Locate the Plasmodium falciparum-infected red blood cells and any of indeterminate infection status.
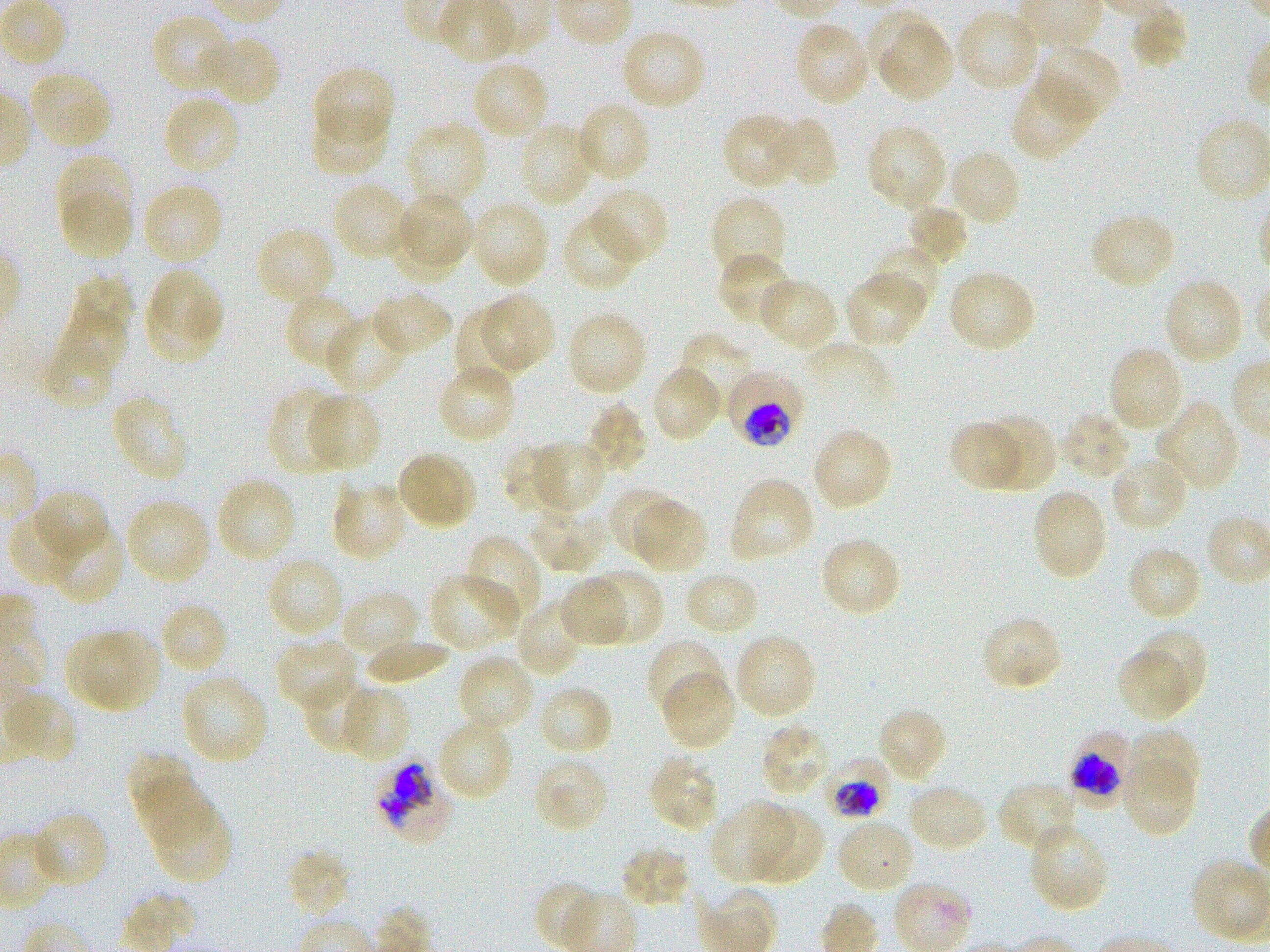
Approximate bounding boxes as {x1, y1, x2, y2} in pixels. Not every red blood cell is marked. A life-cycle stage — or a range of stages, where the recorded stages span more than one — follows each staged infected red blood cell.
Infected red blood cells: {726, 368, 806, 450} trophozoite; {1072, 727, 1135, 809}; {822, 755, 894, 821} trophozoite; {373, 758, 453, 845}.
Red blood cells of indeterminate infection status: {835, 818, 916, 895}.

{
  "locations_of_uninfected_red_blood_cells": "{1129, 7, 1189, 70}, {956, 9, 1041, 92}, {864, 10, 936, 81}, {151, 14, 234, 94}, {793, 21, 871, 107}, {875, 21, 955, 102}, {620, 28, 707, 111}, {201, 34, 281, 108}, {1036, 45, 1123, 125}, {471, 60, 551, 142}, {312, 67, 396, 144}, {27, 70, 113, 149}, {1011, 76, 1095, 161}, {162, 95, 241, 176}, {575, 101, 652, 183}, {310, 104, 391, 177}, {720, 113, 800, 189}, {770, 116, 838, 189}, {404, 119, 489, 208}, {517, 122, 596, 208}, {865, 125, 948, 213}, {948, 148, 1022, 227}, {55, 155, 132, 229}, {332, 181, 409, 262}, {142, 182, 224, 265}, {58, 187, 133, 260}, {590, 187, 669, 264}, {396, 190, 474, 269}, {709, 194, 788, 280}, {471, 200, 550, 287}, {904, 202, 971, 267}, {562, 212, 641, 292}, {1089, 212, 1177, 291}, {394, 218, 457, 285}, {254, 227, 337, 307}, {871, 245, 942, 315}, {716, 253, 794, 326}, {947, 268, 1036, 354}, {149, 269, 224, 340}, {845, 272, 927, 348}, {70, 273, 134, 336}, {757, 277, 839, 352}, {1162, 277, 1245, 366}, {370, 289, 453, 357}, {285, 294, 364, 371}, {480, 294, 556, 374}, {146, 298, 218, 363}, {56, 306, 127, 375}, {452, 307, 519, 383}, {565, 309, 649, 396}, {324, 312, 407, 394}, {676, 334, 752, 412}, {38, 339, 116, 411}, {805, 341, 892, 420}, {1107, 345, 1185, 433}, {436, 363, 517, 445}, {650, 365, 723, 445}, {268, 388, 348, 477}, {307, 391, 383, 472}, {110, 394, 190, 483}, {1154, 400, 1239, 493}, {584, 401, 648, 475}, {1058, 410, 1131, 481}, {983, 413, 1058, 491}, {948, 420, 1024, 492}, {811, 427, 894, 511}, {530, 440, 607, 515}, {500, 441, 565, 513}, {397, 451, 477, 531}, {1110, 455, 1189, 532}, {215, 476, 297, 564}, {729, 477, 815, 562}, {330, 479, 408, 562}, {606, 486, 680, 559}, {1030, 487, 1109, 581}, {33, 490, 110, 562}, {124, 498, 212, 585}, {632, 500, 707, 573}, {527, 504, 610, 574}, {7, 510, 82, 588}, {50, 523, 126, 606}, {464, 535, 542, 623}, {819, 535, 902, 618}, {1125, 546, 1203, 621}, {266, 554, 346, 639}, {590, 569, 665, 645}, {683, 571, 761, 638}, {428, 572, 521, 652}, {560, 576, 632, 647}, {341, 589, 421, 661}, {514, 599, 583, 678}, {159, 602, 230, 676}, {980, 614, 1064, 692}, {84, 628, 163, 712}, {1135, 630, 1207, 709}, {69, 632, 146, 708}, {733, 632, 818, 720}, {273, 638, 360, 713}, {362, 638, 451, 687}, {647, 638, 727, 719}, {1116, 649, 1190, 722}, {457, 654, 536, 734}, {661, 672, 736, 751}, {179, 673, 269, 765}, {302, 679, 380, 754}, {340, 684, 412, 763}, {537, 684, 614, 756}, {2, 692, 80, 765}, {876, 706, 948, 784}, {437, 718, 514, 802}, {758, 721, 831, 797}, {1126, 726, 1201, 798}, {125, 751, 196, 825}, {646, 752, 721, 833}, {531, 756, 610, 833}, {1120, 757, 1196, 838}, {141, 773, 214, 847}, {997, 779, 1077, 853}, {907, 783, 990, 854}, {150, 800, 233, 884}, {709, 804, 792, 884}, {746, 804, 824, 885}, {30, 810, 110, 889}, {1027, 820, 1110, 913}, {618, 845, 692, 911}, {285, 847, 353, 917}, {894, 879, 971, 952}, {534, 881, 599, 950}",
  "preparation": "thin blood film",
  "stain": "Giemsa",
  "image_size": "1270×952 pixels",
  "objective": "100x, oil immersion, numerical aperture 1.25",
  "culture": "in-vitro Plasmodium falciparum strain 3D7, static",
  "field_of_view": "single",
  "donor_blood_group": "O+"
}